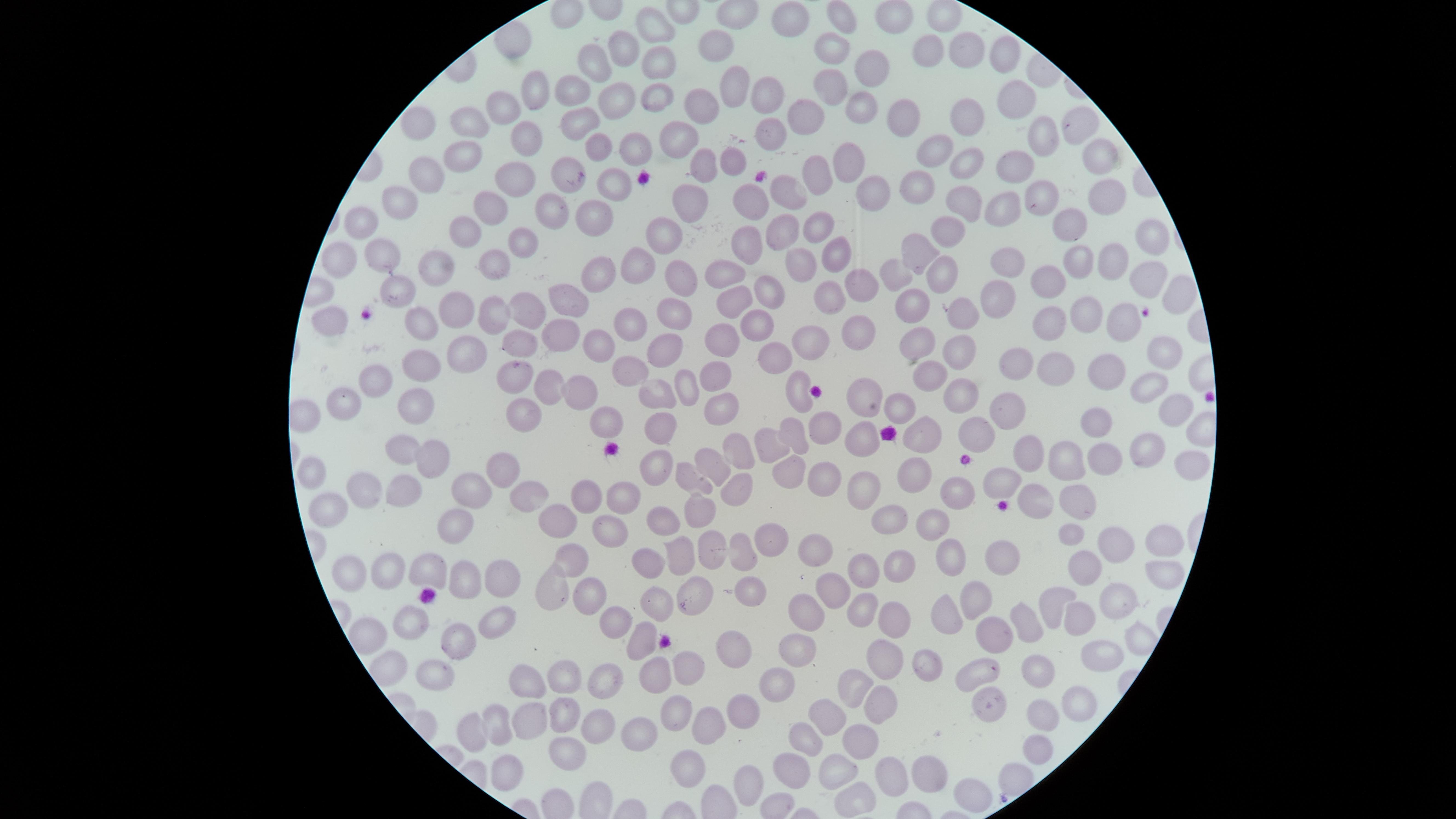
Approximate marker points as (x, y) in pixels.
Summary:
  - Uninfected red blood cells: (899, 9), (951, 10), (839, 13), (791, 17), (659, 18), (714, 44), (831, 45), (925, 48), (624, 49), (967, 49), (1004, 54), (604, 60), (657, 61), (869, 63), (731, 85), (827, 86), (577, 87), (534, 90), (651, 95), (771, 96), (609, 101), (1015, 101), (696, 103), (859, 104), (506, 110), (901, 112), (577, 113), (803, 115), (1080, 119), (471, 121), (415, 122), (968, 122), (674, 132), (770, 133), (1046, 134), (520, 136), (596, 143), (631, 145), (934, 145), (463, 153), (847, 158), (1097, 161), (964, 163), (735, 164), (700, 166), (1010, 170), (426, 174), (818, 174), (570, 175), (513, 178), (922, 180), (610, 184), (790, 186), (870, 187), (1099, 191), (1048, 192), (971, 196), (751, 197), (397, 200), (684, 202), (1000, 203), (487, 206), (592, 206), (556, 207), (362, 216), (1070, 217), (947, 227), (781, 228), (813, 229), (660, 233), (460, 234), (1159, 236), (751, 242), (529, 245), (921, 247), (378, 250), (838, 251), (344, 254), (500, 257), (1082, 257), (1010, 259), (1112, 259), (642, 265), (798, 265), (593, 267), (725, 269), (434, 271), (1144, 273), (937, 274), (885, 277), (680, 278), (1047, 279), (860, 280), (391, 283), (829, 290), (568, 294), (767, 294), (999, 294), (1177, 298), (734, 300), (527, 302), (918, 304), (492, 305), (965, 305), (451, 308), (672, 309), (1084, 312), (325, 317), (628, 317), (1123, 323), (1048, 324), (414, 327), (758, 327), (857, 333), (555, 335), (721, 337), (806, 337), (517, 339), (598, 344), (915, 344), (662, 347), (1159, 352), (461, 353), (961, 353), (1018, 355), (767, 356), (415, 365), (511, 366), (1050, 367), (633, 369), (376, 376), (721, 376), (1110, 376), (547, 379), (928, 379), (1146, 381), (678, 385), (792, 387), (585, 391), (864, 394), (342, 395), (414, 397), (659, 397), (967, 397), (724, 398), (1168, 402), (893, 405), (1012, 407), (524, 408), (613, 419), (662, 424), (825, 424), (1096, 425), (975, 429), (922, 431), (858, 435), (787, 436), (398, 445), (763, 445), (1032, 449), (736, 450), (1138, 452), (429, 456), (711, 458), (652, 460), (1064, 460), (1098, 460), (312, 469), (501, 470), (1189, 471), (789, 475), (917, 477), (1010, 481), (827, 484), (860, 487), (735, 488), (359, 489), (403, 491), (475, 492), (958, 494), (631, 496), (526, 497), (1080, 497), (588, 498), (1035, 499), (329, 506), (696, 512), (890, 514), (664, 521), (554, 522), (458, 524), (933, 528), (612, 534), (1075, 538), (1162, 538), (770, 539), (1121, 546), (707, 547), (813, 548), (742, 550), (573, 554), (679, 554), (947, 555), (996, 560), (858, 565), (342, 566), (503, 566), (653, 566), (383, 567), (896, 568), (1158, 570), (426, 571), (1083, 573), (463, 582), (830, 588), (750, 591), (693, 592), (545, 593), (586, 594), (970, 596), (662, 597), (1061, 598), (1114, 601), (859, 607), (804, 613), (1031, 613), (939, 614), (492, 618), (1080, 618), (616, 619), (894, 622), (414, 624), (997, 629), (367, 630), (1135, 636), (644, 640), (456, 647), (730, 650), (1112, 651), (792, 652), (884, 658), (684, 662), (930, 664), (1035, 665), (387, 667), (979, 667), (431, 668), (656, 673), (603, 676), (563, 677), (532, 680), (776, 684), (853, 685), (986, 702), (1075, 706), (877, 707), (563, 711), (672, 712), (745, 712), (827, 712), (1042, 714), (529, 720), (500, 724), (472, 728), (706, 728), (603, 731), (810, 732), (644, 734), (855, 742), (1034, 754), (566, 755), (685, 763), (503, 767), (793, 769), (829, 771), (890, 771), (929, 778), (751, 781), (968, 788), (851, 801)
  - Stain: Giemsa
  - Visible region: circular
  - Image size: 1456×819 pixels
  - Field of view: single
  - Preparation: thin blood smear
  - Capture: smartphone photograph through the microscope eyepiece
  - Presence: no malaria parasites identified